Assess this cell for malaria.
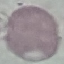
Uninfected.

Thin blood smear. Automatically extracted cell patch, resized to 64 × 64 pixels. Giemsa stain. Acquired by smartphone through the microscope eyepiece.